Outline each blood parasite and name the species.
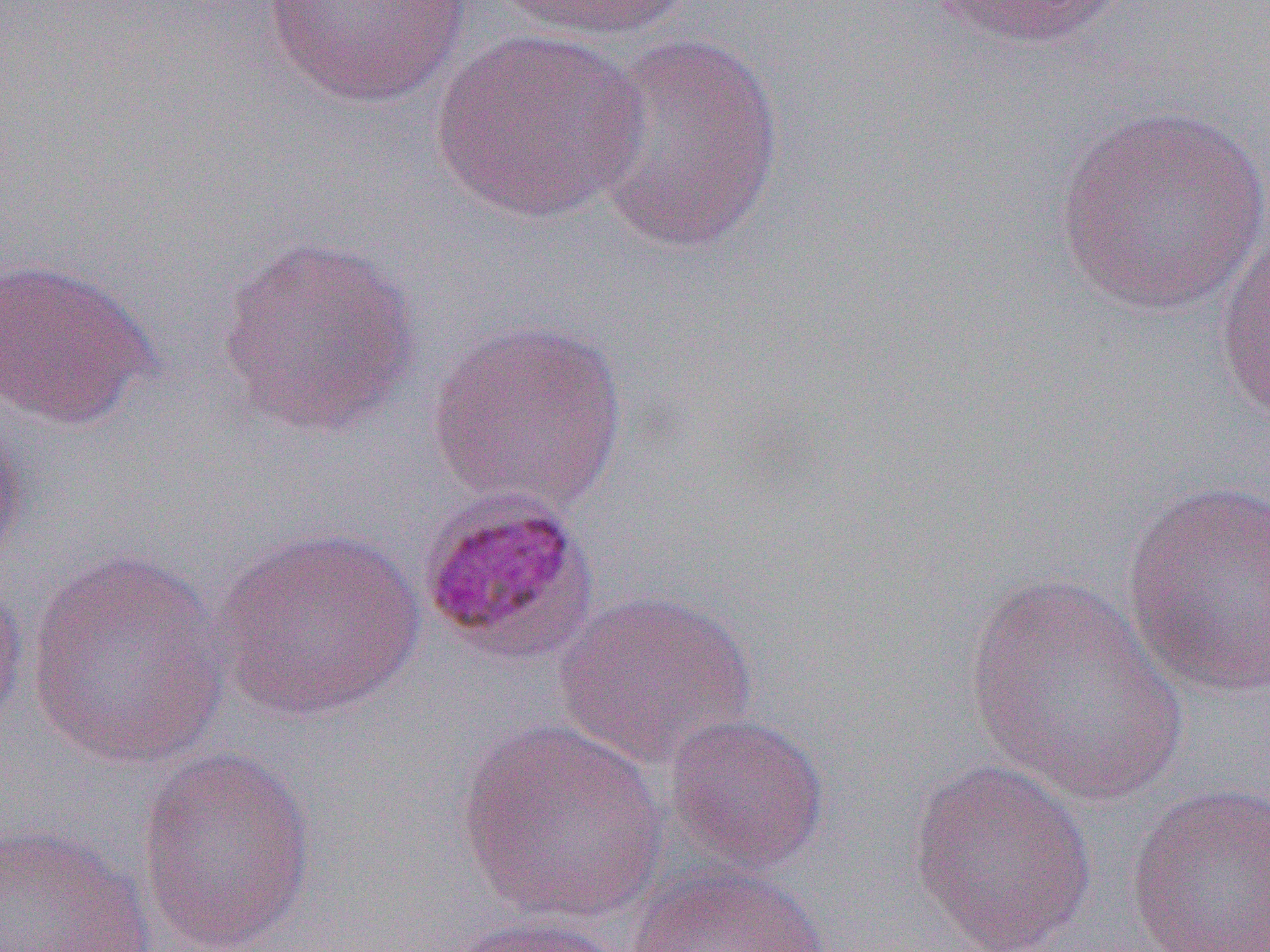
Approximate bounding boxes as (x1,y1)-(x2,y2) corner pairs in pixels.
Plasmodium malariae-infected red blood cells: (415,491)-(600,668).
No Plasmodium falciparum, Plasmodium ovale, Plasmodium vivax, Babesia divergens, or Trypanosoma brucei observed.

Uninfected red blood cell locations: (259,0)-(471,109), (489,0)-(697,44), (928,0)-(1128,52), (432,27)-(647,225), (587,32)-(785,254), (1051,105)-(1270,318), (1213,223)-(1270,428), (215,234)-(424,438), (0,256)-(160,430), (425,317)-(630,512), (0,409)-(30,573), (1120,479)-(1270,698), (214,525)-(426,723), (22,549)-(232,771), (0,568)-(29,734), (959,574)-(1188,806), (555,589)-(759,771), (662,711)-(830,876), (455,719)-(671,925), (135,745)-(318,952), (907,758)-(1099,952), (1124,781)-(1270,952), (0,822)-(155,952), (623,861)-(829,952), (441,914)-(628,952). Slide-level diagnosis: Plasmodium malariae. Thin blood film. 1000x magnification. Image is 1270×952 pixels. Light microscopy. Single field of view.